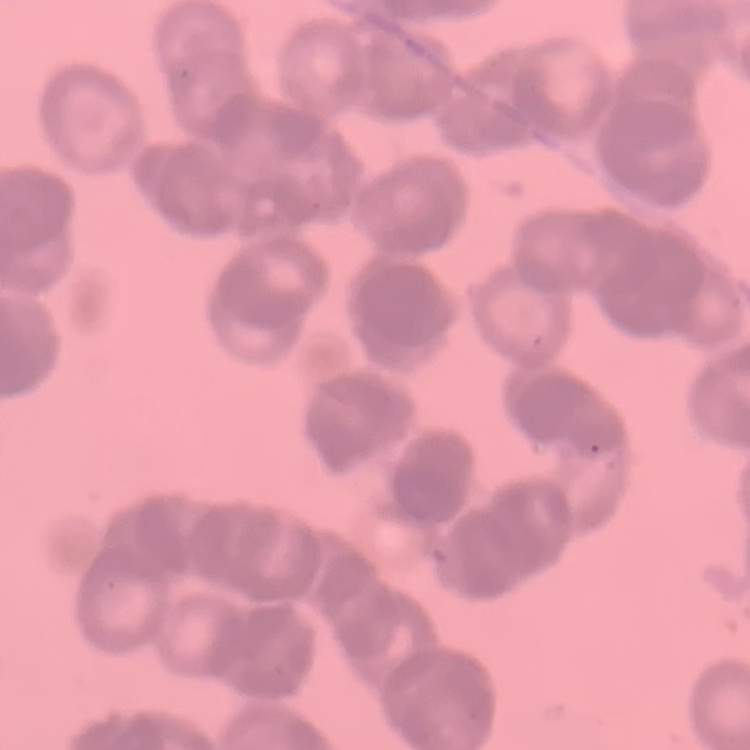
Summary:
  - Red blood cell morphology: rouleaux formation
  - Stain: Field's or Giemsa
  - Image type: one tile cut from a larger photomicrograph
  - Preparation: thin blood film